Identify the blood parasite species.
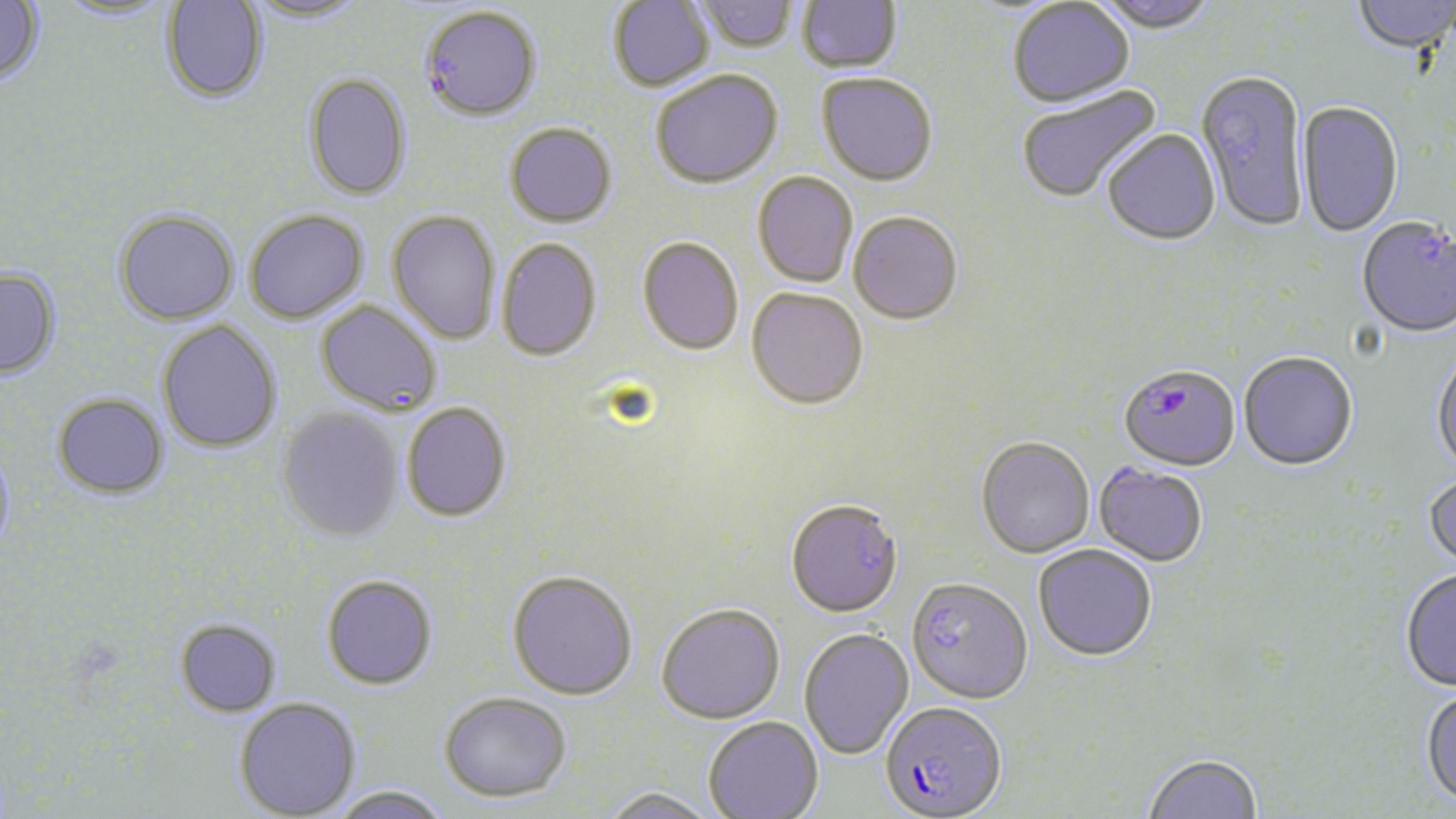
Plasmodium falciparum.

Approximate bounding boxes as (x1, y1, x2, y2) in pixels. Plasmodium falciparum-infected red blood cell locations: (1119, 363, 1240, 471), (880, 700, 1007, 819). Uninfected red blood cell locations: (0, 0, 45, 84), (161, 0, 268, 103), (244, 0, 369, 23), (608, 0, 714, 92), (694, 0, 798, 53), (797, 0, 902, 73), (1095, 0, 1220, 32), (1353, 0, 1455, 54), (54, 1, 175, 22), (1008, 1, 1134, 107), (420, 6, 541, 121), (1196, 67, 1309, 232), (651, 69, 783, 189), (302, 72, 412, 201), (817, 72, 938, 186), (1016, 85, 1162, 205), (1297, 99, 1404, 237), (505, 123, 617, 227), (1102, 128, 1220, 246), (752, 171, 858, 288), (114, 209, 239, 325), (244, 209, 368, 324), (387, 210, 501, 344), (848, 211, 963, 325), (1357, 215, 1456, 337), (496, 237, 602, 362), (637, 237, 744, 356), (0, 267, 61, 380), (745, 287, 868, 410), (316, 300, 441, 416), (157, 320, 282, 454), (1239, 351, 1358, 470), (1430, 351, 1456, 475), (52, 393, 169, 499), (401, 402, 512, 522), (277, 406, 404, 543), (976, 436, 1095, 559), (0, 445, 16, 561), (1093, 463, 1208, 567), (1424, 472, 1456, 572), (785, 498, 903, 618), (1033, 544, 1157, 661), (1400, 569, 1456, 691), (507, 570, 638, 700), (321, 574, 438, 690), (906, 576, 1033, 704), (656, 603, 785, 724), (174, 618, 281, 717), (799, 628, 913, 760), (1421, 686, 1456, 809), (439, 691, 571, 803), (234, 697, 361, 819), (703, 716, 824, 819), (1142, 752, 1263, 819), (330, 785, 452, 819), (601, 786, 719, 819). 1000x magnification. May-Grünwald-Giemsa-stained preparation. Light microscopy. Single field of view. Image is 1456×819 pixels. Thin blood smear.